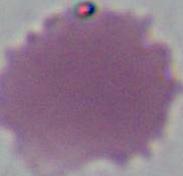
Summary:
  - Modality: photomicrograph
  - Identification: red blood cell
  - Magnification: 1000x